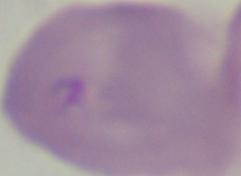

Summary:
  - Magnification: 1000x
  - Identification: Babesia
  - Modality: micrograph